Classify this cell by malaria status.
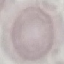
It is uninfected.

Summary:
  - Stain: Giemsa
  - Preparation: thin blood smear
  - Image type: automatically extracted cell patch, resized to 64 × 64 pixels
  - Capture: smartphone through the microscope eyepiece